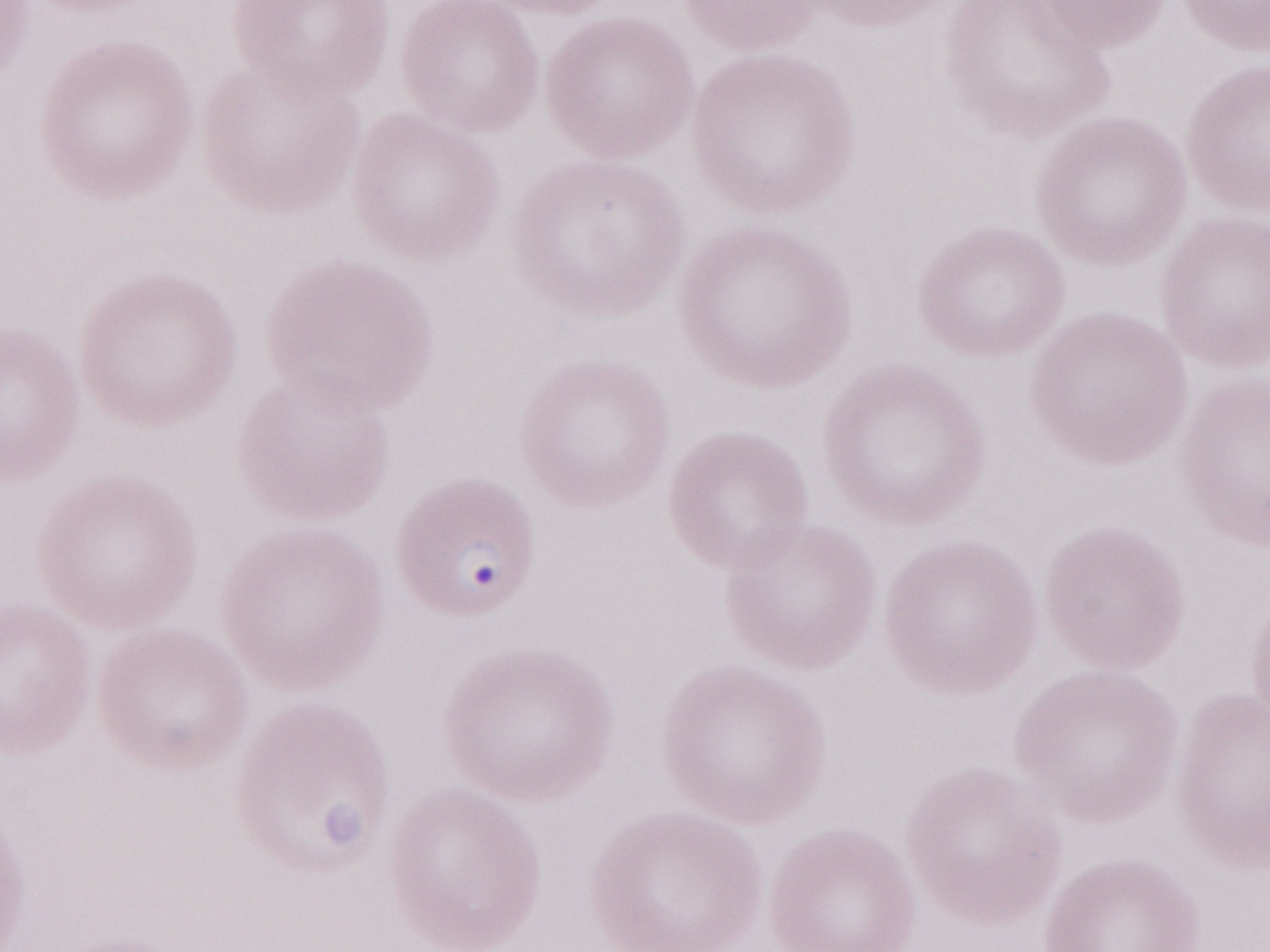
Image is 1270×952 pixels. Thin peripheral-blood smear. May-Grünwald-Giemsa (MGG) stain. Olympus BX43 microscope and DP73 digital camera. Single field of view. 1,000x magnification. Patient-level malaria diagnosis: positive.